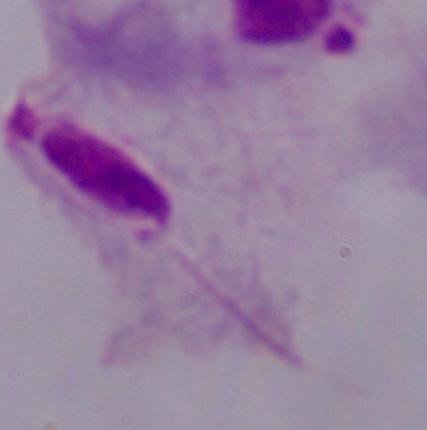
A trichomonad is seen. Micrograph. 1000x magnification.